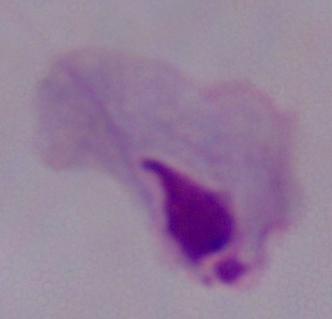

Captured at 1000x magnification. A trichomonad is seen. Micrograph.